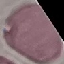
Summary:
  - Result: no malaria parasites seen
  - Capture: smartphone camera at the microscope eyepiece
  - Preparation: thin blood smear
  - Image type: automatically extracted cell patch, resized to 64 × 64 pixels
  - Stain: Giemsa